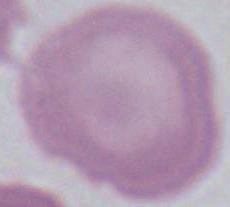
identification = red blood cell
magnification = 1000x
modality = micrograph